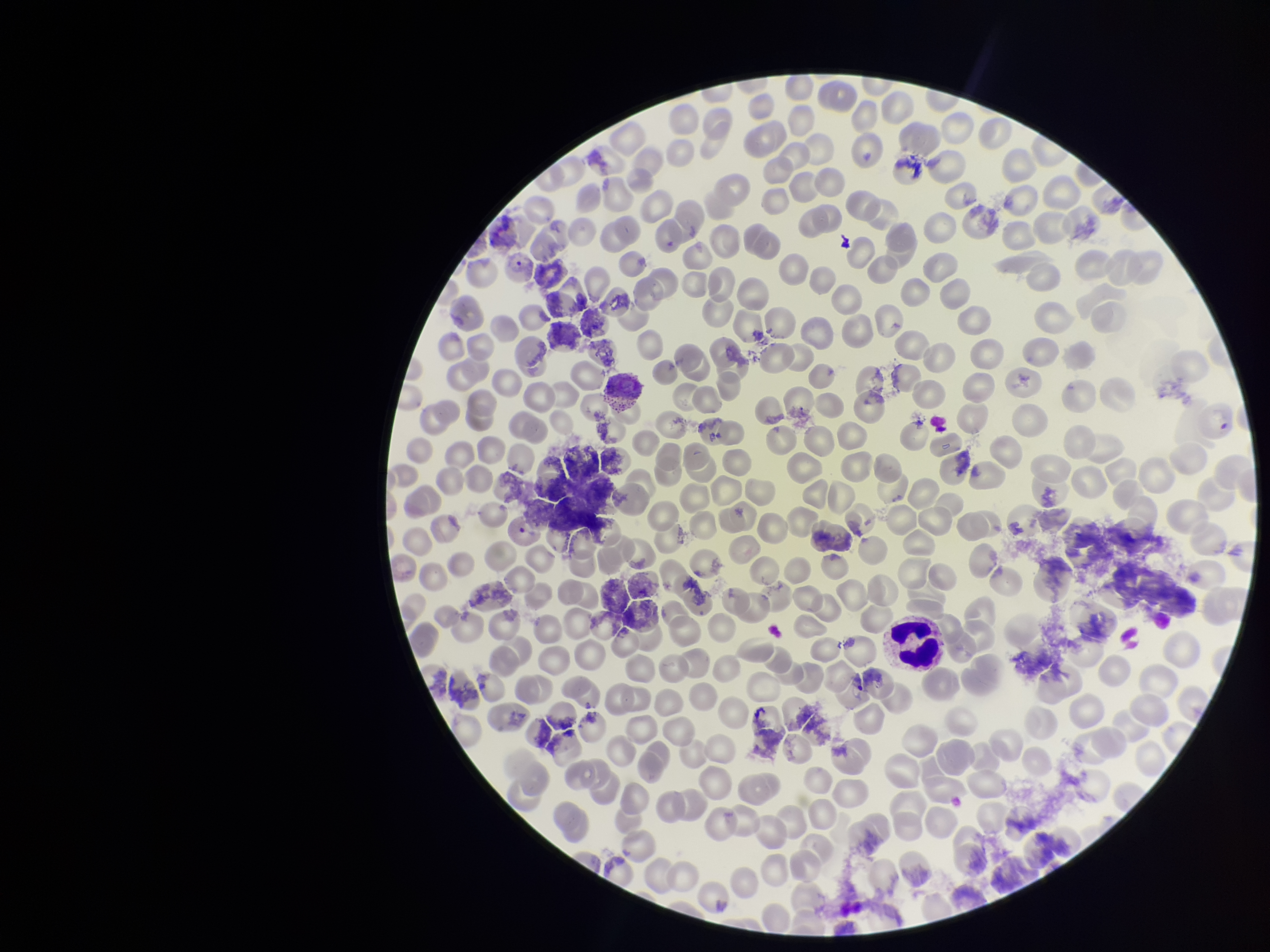

Patient malaria status: infected. Preparation: thin blood smear. Red blood cell count: 172. Stained with Giemsa. Species reported for this patient: Plasmodium vivax. Parasitized red blood cell count: 0. One field from this slide. Smartphone photograph taken through the eyepiece of a microscope. Image is 1270×952 pixels. Parasitized red blood cells: none identified.